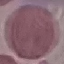
Result: no malaria parasites seen. Cell patch, automatically extracted from a larger field of view and resized to 64 × 64 pixels. Giemsa stain. Thin blood smear. Photographed with a smartphone camera at the microscope eyepiece.